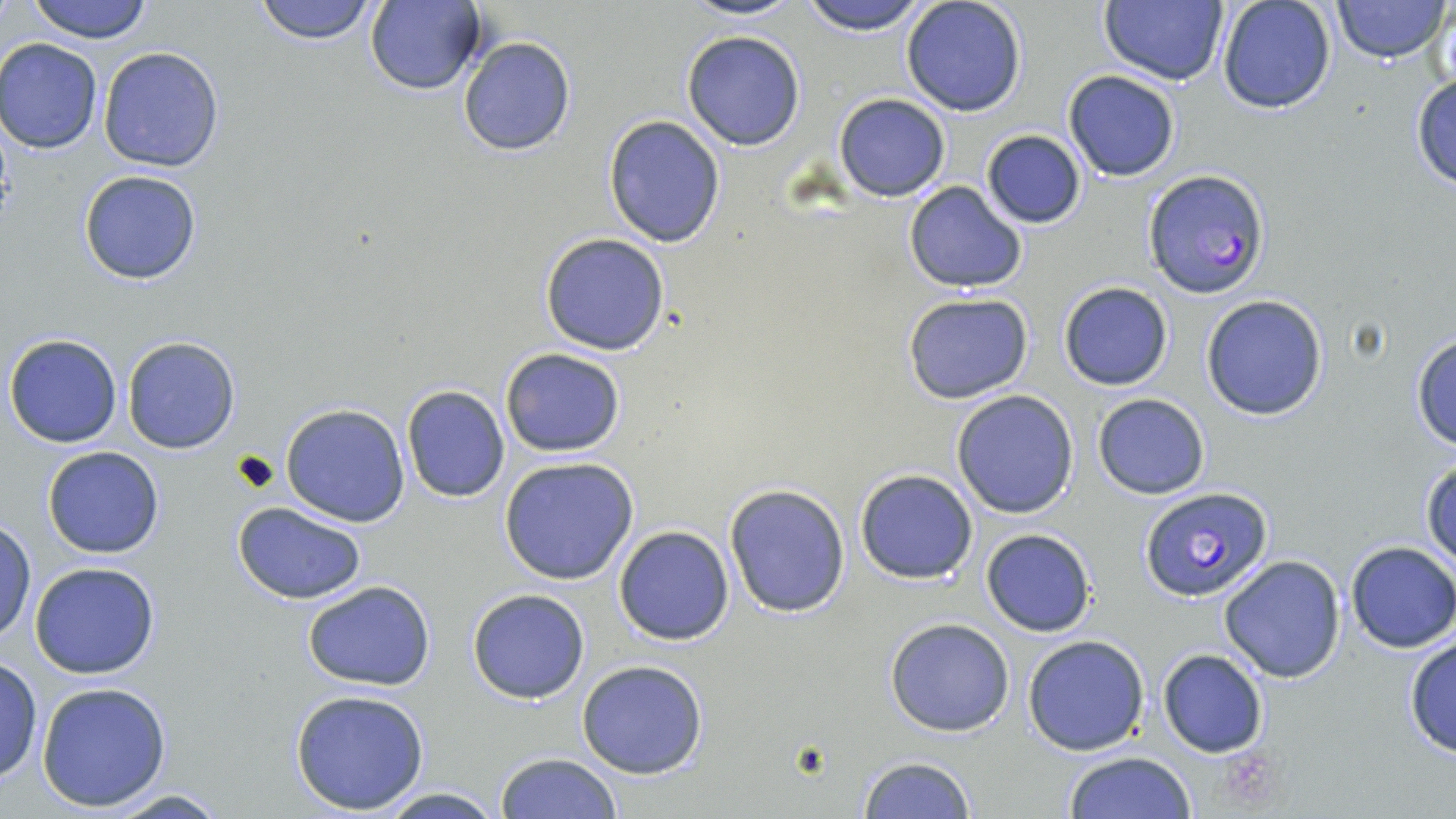

Plasmodium falciparum-infected red blood cell locations = approximate bounding boxes as (x1,y1)-(x2,y2) corner pairs in pixels: (1145,169)-(1270,299), (1138,487)-(1273,602)
slide-level diagnosis = Plasmodium falciparum
field of view = one of a larger specimen
preparation = thin blood smear
stain = May-Grünwald-Giemsa
image size = 1456×819 pixels
magnification = 1000x
modality = light microscopy
uninfected red blood cell locations = approximate bounding boxes as (x1,y1)-(x2,y2) corner pairs in pixels: (25,0)-(156,43), (682,0)-(804,22), (798,0)-(933,33), (900,0)-(1028,117), (1100,0)-(1227,87), (1331,0)-(1452,63), (250,1)-(381,45), (364,1)-(486,96), (1217,1)-(1337,115), (681,30)-(805,149), (457,36)-(577,156), (1,38)-(103,153), (97,47)-(226,174), (1063,69)-(1181,182), (1410,71)-(1456,189), (833,94)-(951,202), (603,115)-(726,247), (981,130)-(1085,229), (79,169)-(202,284), (903,181)-(1029,294), (538,233)-(671,355), (1057,281)-(1174,391), (901,293)-(1034,404), (1201,295)-(1329,420), (1409,332)-(1456,451), (5,333)-(123,448), (122,336)-(240,454), (500,349)-(626,457), (400,386)-(510,502), (950,390)-(1079,519), (1092,392)-(1210,499), (281,403)-(410,527), (43,446)-(165,559), (499,456)-(640,584), (1423,458)-(1456,567), (854,468)-(979,585), (723,483)-(851,618), (233,503)-(368,602), (0,518)-(36,644), (613,526)-(736,645), (980,529)-(1097,637), (1345,540)-(1456,652), (1218,555)-(1347,683), (29,563)-(160,679), (300,580)-(438,691), (467,589)-(590,705), (884,617)-(1015,737), (1403,633)-(1456,760), (1022,636)-(1149,755), (1156,648)-(1268,758), (0,657)-(44,783), (576,659)-(709,779), (36,681)-(172,812), (290,689)-(432,814), (1062,751)-(1197,819), (496,752)-(622,819), (857,756)-(978,818), (375,786)-(506,819), (96,787)-(236,819)